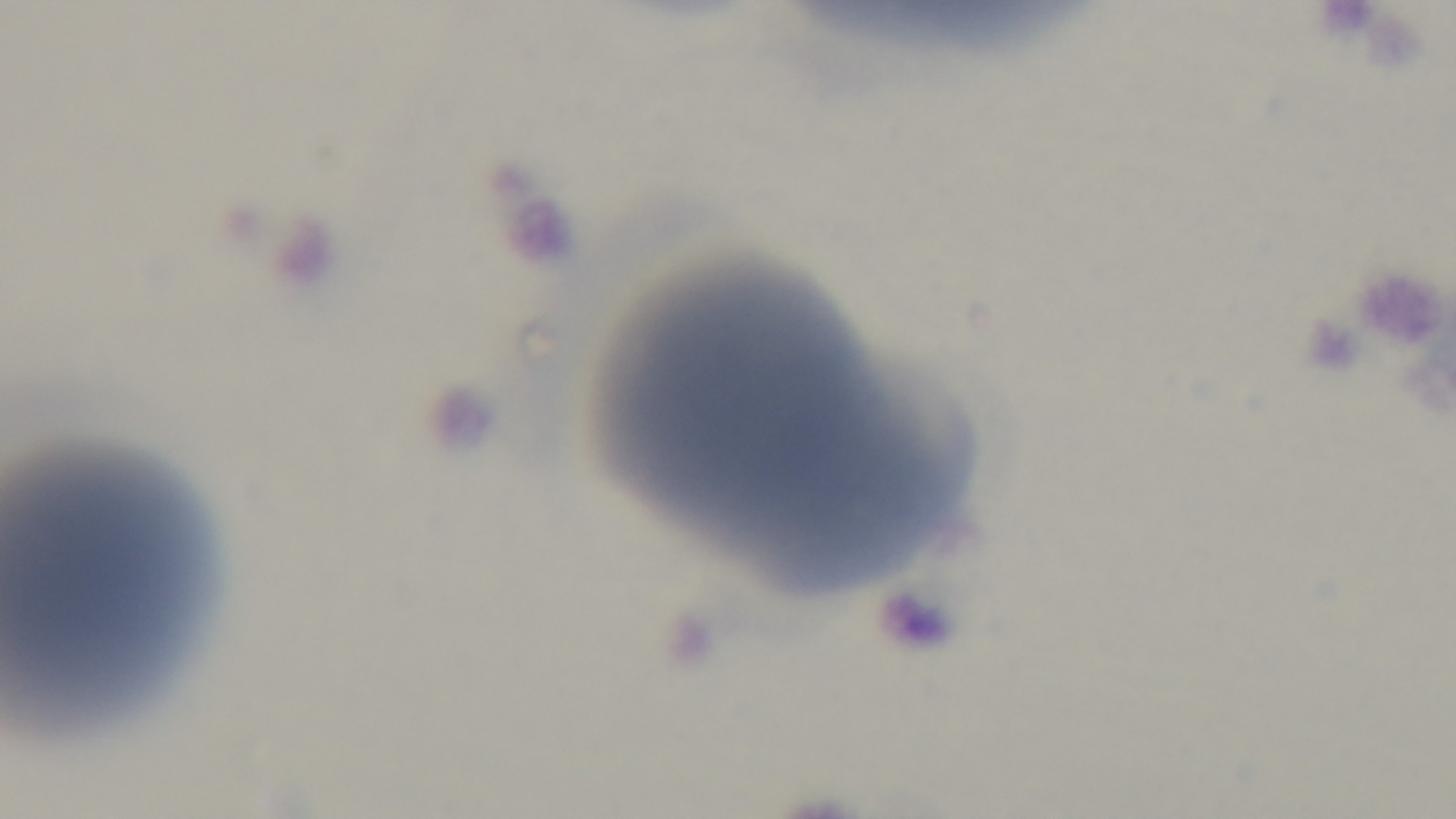
Giemsa stain. Preparation: thin blood film. Malaria status: negative. 100x oil-immersion objective. Light microscopy. Single field of view. Captured with a mounted 4K digital camera.